Assess for Plasmodium parasites.
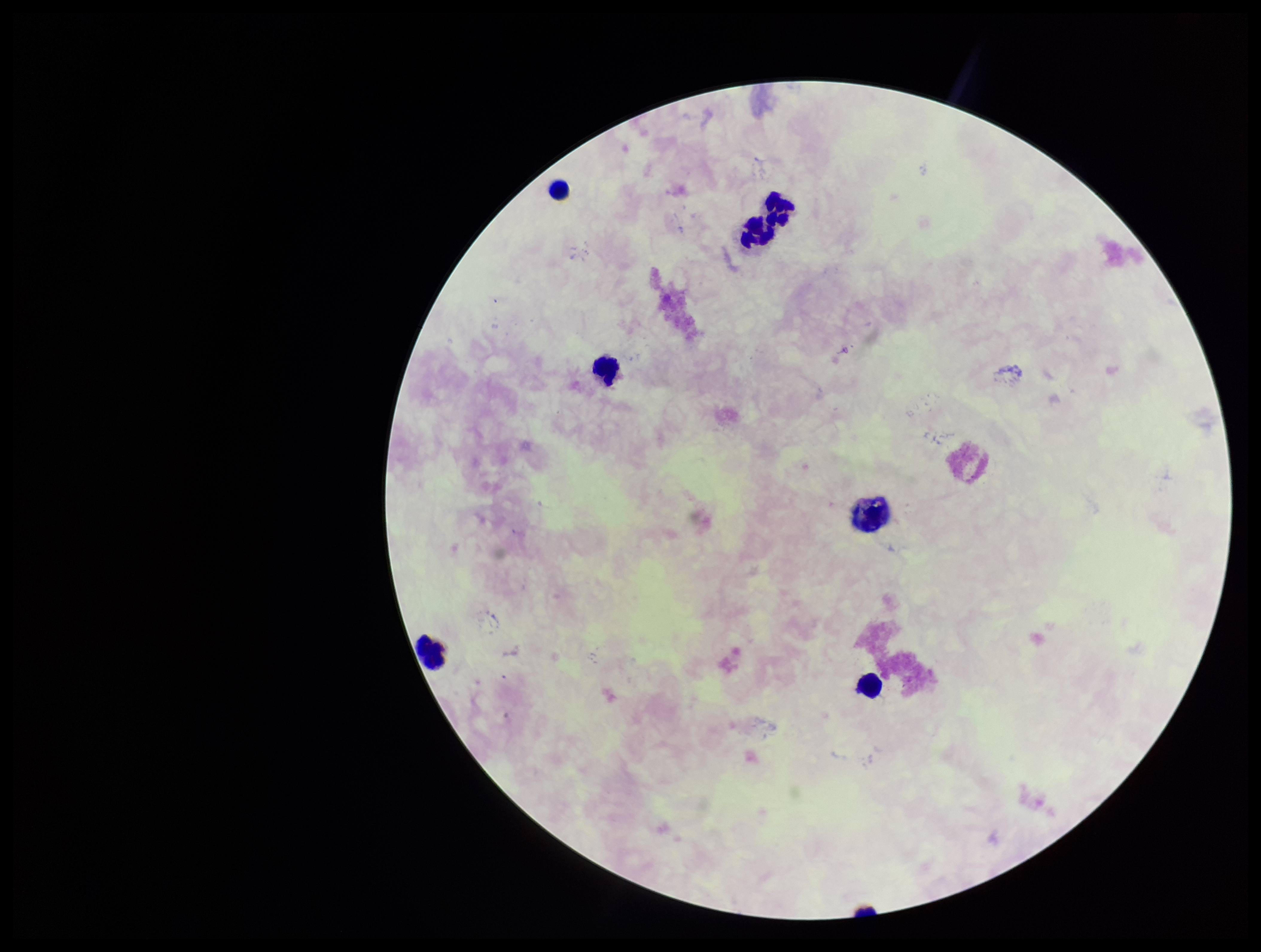

None seen.

parasite_count: 0
preparation: thick smear
capture: smartphone photograph through the microscope eyepiece
image_size: 1261×952 pixels
field_of_view: single
patient_malaria_status: negative
stain: Giemsa
leukocyte_count: 7